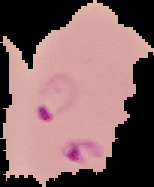
Summary:
  - Preparation: thin blood smear
  - Image type: segmented cell region on a black background
  - Malaria status: parasitized
  - Image size: 154×187 pixels